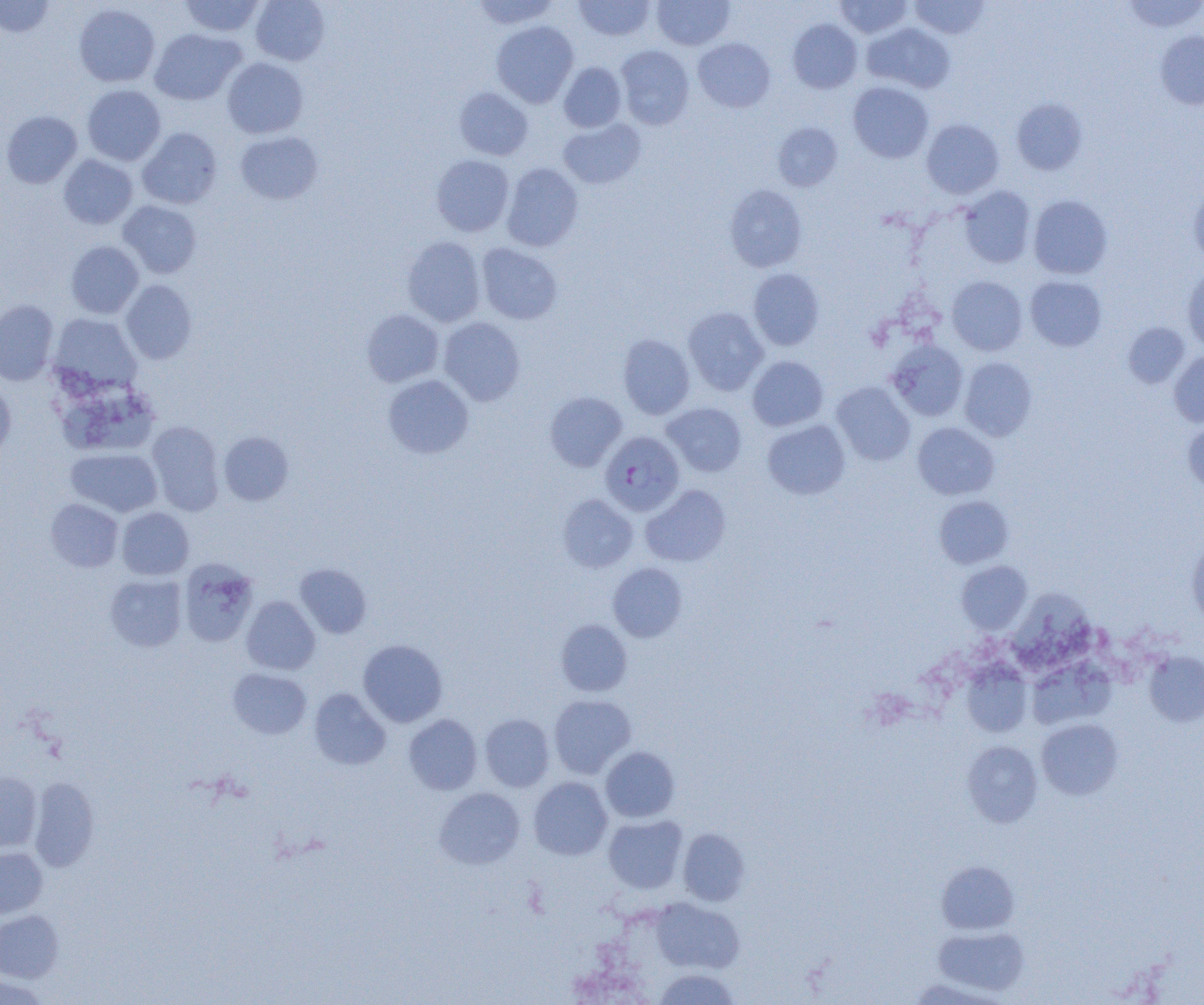
slide-level diagnosis = Plasmodium falciparum
preparation = thin blood smear
Plasmodium falciparum-infected red blood cell locations = approximate bounding boxes as (x1, y1, x2, y2) in pixels: (600, 431, 685, 516)
field of view = one of a larger specimen
uninfected red blood cell locations = approximate bounding boxes as (x1, y1, x2, y2) in pixels: (0, 0, 55, 38), (180, 0, 265, 37), (251, 0, 330, 65), (471, 0, 560, 30), (574, 0, 655, 41), (652, 0, 734, 50), (834, 0, 913, 38), (910, 0, 990, 39), (1122, 0, 1204, 33), (74, 4, 160, 87), (787, 18, 863, 94), (491, 21, 579, 107), (862, 22, 955, 93), (149, 29, 245, 105), (1155, 30, 1204, 109), (693, 38, 776, 113), (615, 45, 694, 130), (222, 58, 308, 138), (558, 61, 626, 132), (848, 81, 934, 163), (83, 85, 166, 166), (454, 87, 533, 160), (1011, 97, 1088, 175), (1, 111, 82, 188), (558, 119, 646, 189), (921, 119, 1004, 199), (773, 123, 842, 191), (137, 127, 222, 209), (236, 131, 323, 204), (431, 154, 514, 236), (58, 155, 138, 229), (501, 163, 583, 252), (725, 184, 808, 272), (1188, 185, 1204, 267), (960, 186, 1036, 268), (1028, 195, 1112, 279), (118, 201, 201, 278), (402, 236, 485, 327), (66, 241, 143, 318), (477, 243, 563, 324), (1182, 267, 1204, 352), (748, 268, 825, 351), (946, 276, 1027, 355), (1025, 276, 1106, 351), (121, 280, 197, 364), (0, 300, 59, 385), (683, 307, 768, 396), (361, 309, 443, 387), (49, 314, 140, 394), (439, 317, 525, 405), (1122, 322, 1190, 387), (618, 333, 695, 419), (886, 340, 968, 421), (1168, 351, 1204, 427), (747, 355, 829, 430), (958, 357, 1037, 441), (383, 374, 474, 458), (0, 381, 16, 460), (832, 382, 915, 465), (59, 391, 171, 460), (545, 391, 627, 471), (662, 402, 747, 477), (762, 420, 850, 499), (146, 421, 225, 515), (1183, 421, 1204, 494), (912, 422, 999, 500), (219, 431, 294, 506), (65, 448, 162, 517), (640, 484, 730, 567), (557, 494, 638, 573), (934, 495, 1013, 569), (46, 498, 123, 572), (116, 507, 194, 580), (1186, 539, 1204, 626), (178, 559, 258, 647), (957, 560, 1032, 634), (607, 562, 687, 642), (295, 563, 372, 638), (105, 575, 187, 652), (1010, 590, 1096, 670), (241, 596, 320, 675), (556, 619, 632, 696), (358, 639, 448, 727), (1143, 651, 1204, 726), (1027, 659, 1116, 730), (962, 661, 1032, 737), (228, 668, 311, 739), (309, 688, 391, 770), (548, 694, 636, 778), (403, 714, 483, 795), (480, 714, 555, 791), (1037, 719, 1123, 799), (961, 740, 1043, 827), (601, 746, 680, 822), (0, 771, 42, 852), (528, 777, 613, 860), (29, 778, 99, 871), (433, 787, 525, 870), (604, 815, 687, 894), (678, 828, 749, 906), (0, 847, 48, 918), (936, 861, 1019, 934), (652, 897, 744, 975), (0, 910, 64, 983), (933, 925, 1029, 996), (653, 969, 740, 1004), (0, 974, 50, 1004)
modality = light microscopy
image size = 1204×1005 pixels
magnification = 1000x